Name the parasite shown.
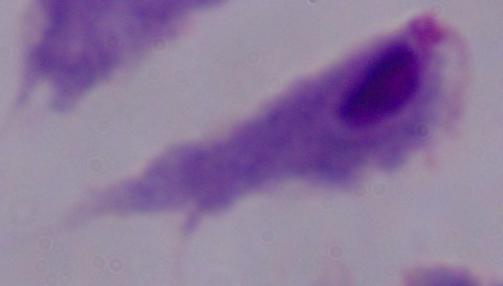

This is a trichomonad.

Summary:
  - Magnification: 1000x
  - Modality: micrograph